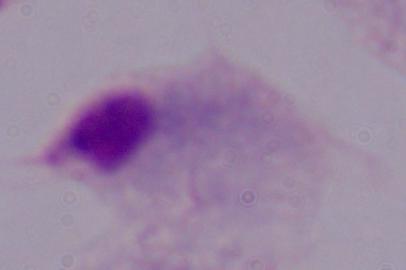
Summary:
  - Magnification: 1000x
  - Modality: micrograph
  - Identification: trichomonad